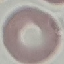

Result: no malaria parasites detected. Acquired by smartphone through the microscope eyepiece. Thin blood film. Cell patch, automatically extracted from a larger field of view and resized to 64 × 64 pixels. Giemsa stain.